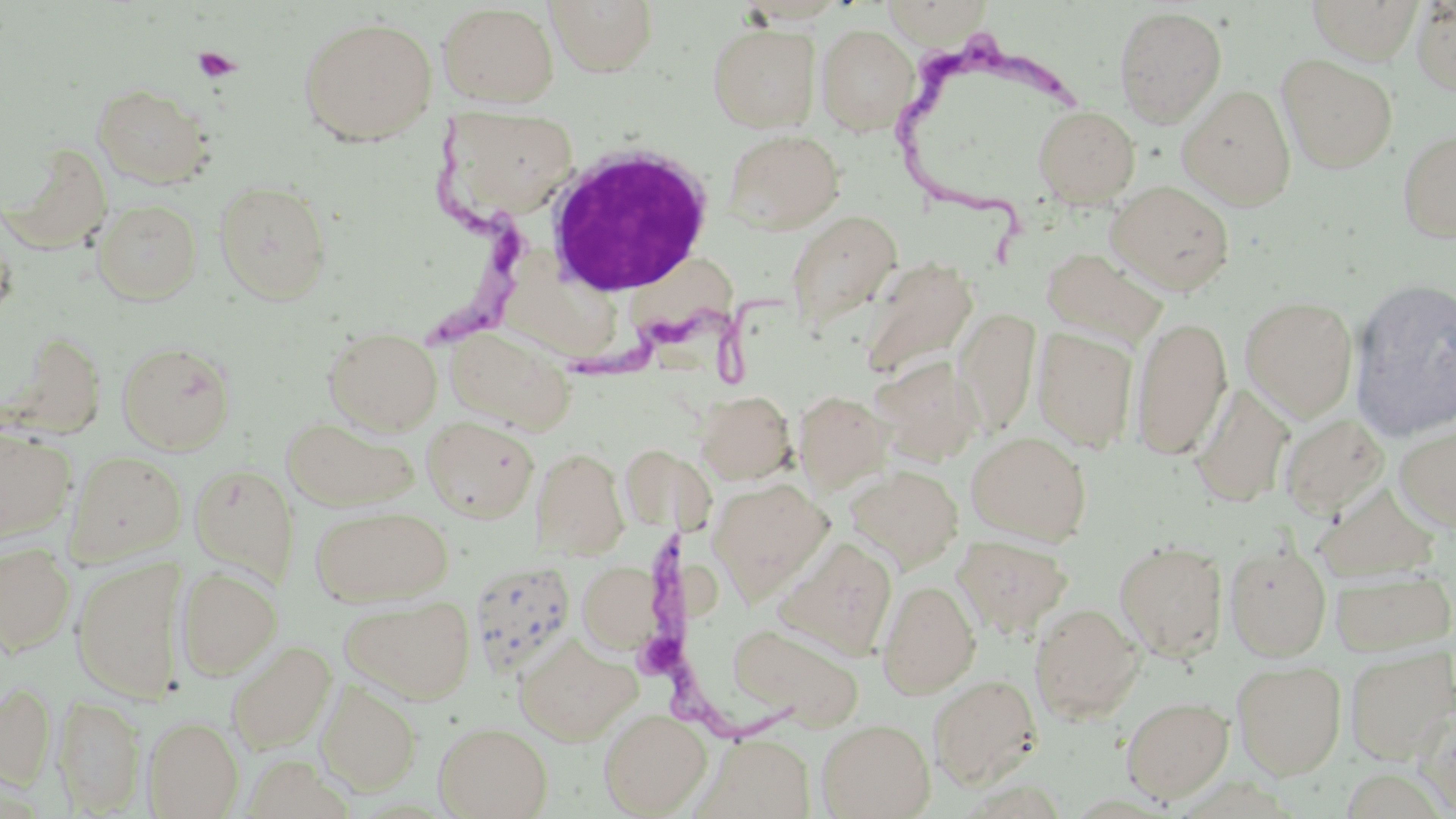

{
  "slide_level_diagnosis": "Trypanosoma brucei",
  "preparation": "thin blood smear",
  "platelet_locations": "approximate bounding boxes as (x1, y1, x2, y2) in pixels: (194, 47, 240, 82)",
  "stain": "May-Grünwald-Giemsa",
  "field_of_view": "single",
  "white_blood_cell_locations": "approximate bounding boxes as (x1, y1, x2, y2) in pixels: (544, 141, 715, 298)",
  "uninfected_red_blood_cell_locations": "approximate bounding boxes as (x1, y1, x2, y2) in pixels: (546, 0, 659, 76), (1305, 0, 1424, 64), (881, 1, 994, 46), (1412, 1, 1456, 98), (436, 3, 559, 108), (1113, 5, 1228, 127), (298, 15, 438, 145), (708, 23, 821, 133), (816, 23, 919, 135), (1276, 53, 1398, 173), (92, 83, 214, 189), (1177, 83, 1297, 210), (1032, 105, 1140, 206), (443, 108, 580, 223), (1396, 125, 1456, 245), (722, 128, 845, 234), (6, 144, 114, 252), (213, 179, 333, 304), (1106, 180, 1235, 295), (92, 199, 203, 304), (785, 210, 901, 332), (0, 221, 17, 321), (1041, 247, 1167, 349), (860, 258, 978, 380), (1349, 276, 1456, 442), (1240, 295, 1358, 421), (956, 308, 1041, 436), (1130, 316, 1232, 459), (444, 325, 575, 433), (322, 326, 443, 435), (1032, 326, 1138, 453), (117, 340, 236, 454), (873, 356, 985, 466), (1191, 384, 1294, 508), (696, 390, 796, 484), (793, 390, 893, 492), (1279, 413, 1390, 519), (282, 416, 419, 512), (422, 417, 539, 522), (1394, 425, 1456, 533), (0, 427, 76, 541), (967, 431, 1092, 544), (620, 444, 690, 532), (531, 447, 629, 559), (66, 450, 186, 563), (188, 462, 299, 585), (845, 464, 964, 572), (709, 478, 833, 601), (1315, 484, 1439, 581), (310, 504, 453, 606), (952, 533, 1073, 638), (776, 536, 898, 659), (1115, 539, 1229, 661), (1225, 542, 1332, 661), (0, 543, 76, 655), (71, 557, 188, 702), (467, 558, 577, 679), (578, 561, 662, 655), (176, 566, 283, 680), (1330, 567, 1455, 655), (877, 579, 981, 698), (339, 593, 476, 705), (1029, 603, 1145, 724), (727, 622, 864, 729), (513, 632, 641, 746), (226, 640, 337, 753), (1345, 647, 1455, 763), (1232, 660, 1347, 778), (929, 673, 1042, 789), (316, 678, 422, 796), (0, 681, 57, 788), (54, 695, 145, 815), (1121, 695, 1234, 803), (1417, 707, 1456, 815), (598, 709, 712, 816), (143, 716, 243, 818), (816, 718, 935, 819), (433, 720, 553, 819), (698, 733, 815, 818)",
  "trypanosoma_brucei_locations": "approximate bounding boxes as (x1, y1, x2, y2) in pixels: (890, 26, 1093, 267), (406, 100, 539, 355), (552, 286, 786, 412), (641, 528, 812, 753)",
  "image_size": "1456×819 pixels",
  "modality": "light microscopy",
  "magnification": "1000x"
}